Identify the parasite.
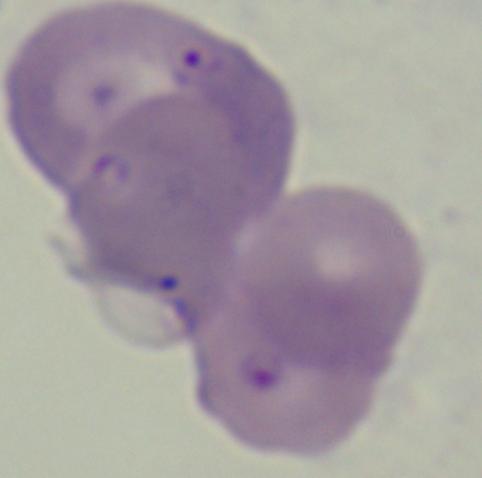

This is Babesia.

{
  "magnification": "1000x",
  "modality": "micrograph"
}